Report the malaria status of this cell.
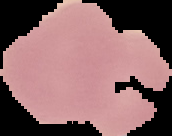
Uninfected.

From a thin blood film. Segmented cell region on a black background. Image is 172×136 pixels.